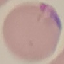

Result: malaria parasites detected. Giemsa stain. Cell patch, automatically extracted from a larger field of view and resized to 64 × 64 pixels. Thin blood smear. Photographed with a smartphone camera at the microscope eyepiece.